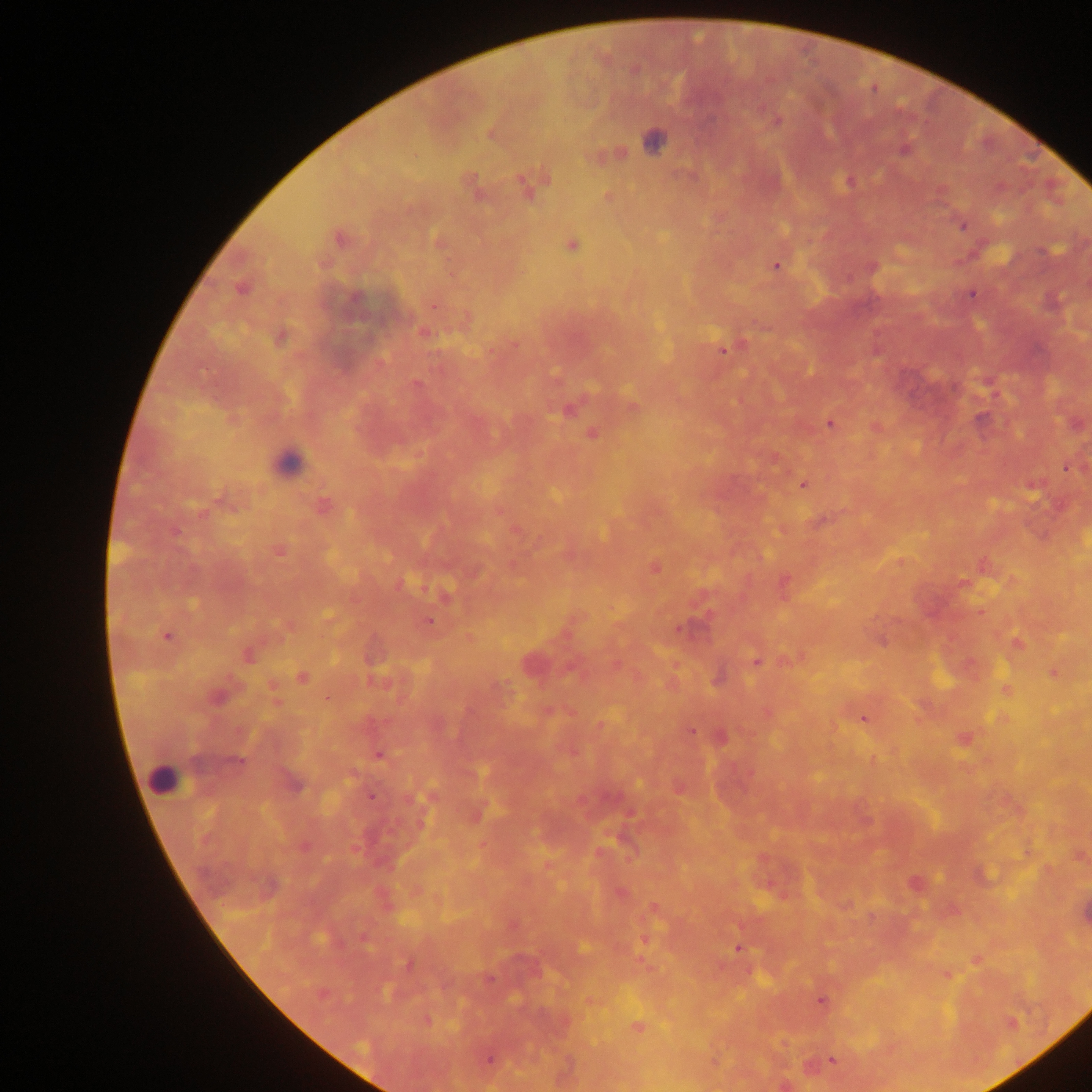
leukocyte locations = approximate centers as (x, y) in pixels: (288, 462), (164, 781)
country = Ghana
Plasmodium parasite locations = approximate centers as (x, y) in pixels: (761, 106), (778, 120), (491, 133), (654, 141), (904, 149), (608, 155), (848, 182), (470, 185), (529, 185), (608, 196), (962, 225), (340, 238), (437, 241), (571, 244), (776, 265), (241, 287), (972, 293), (434, 305), (423, 331), (280, 337), (513, 344), (727, 347), (415, 383), (633, 406), (568, 408), (829, 423), (875, 428), (592, 434), (1069, 467), (802, 483), (1032, 484), (322, 505), (498, 510), (820, 521), (516, 530), (278, 550), (900, 561), (984, 565), (654, 567), (785, 582), (962, 583), (446, 595), (980, 611), (327, 616), (429, 621), (166, 636), (1016, 643), (246, 654), (794, 658), (756, 660), (530, 663), (1055, 673), (302, 677), (718, 679), (1005, 689), (216, 696), (276, 700), (547, 711), (767, 713), (863, 718), (600, 726), (690, 731), (721, 737), (964, 739), (378, 754), (872, 759), (292, 783), (679, 788), (371, 795), (429, 796), (476, 813), (1027, 851), (1079, 856), (548, 864), (981, 875), (914, 883), (620, 892), (653, 907), (953, 910), (644, 938), (582, 948), (737, 948), (976, 959), (409, 964), (947, 974), (321, 993), (589, 1000), (821, 1000), (426, 1020), (637, 1027), (489, 1059), (831, 1059), (714, 1062), (784, 1084)
image size = 1092×1092 pixels
field of view = single
capture = mobile-phone photograph through a microscope
preparation = thick blood film